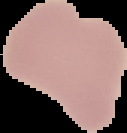

image size = 127×133 pixels
preparation = thin blood smear
malaria status = uninfected
image type = segmented cell region with the area outside set to black